Give the position of every Plasmodium parasite visible.
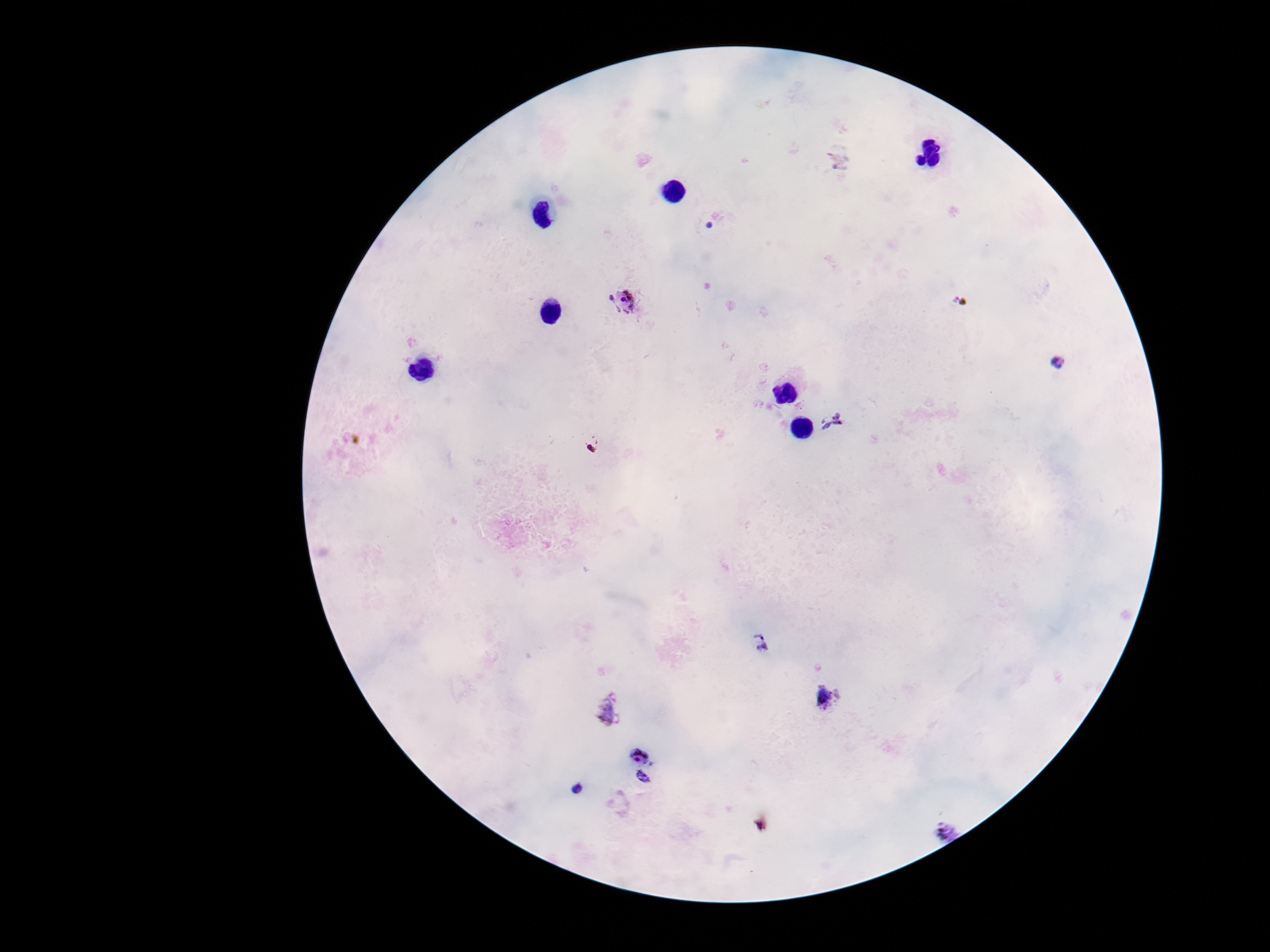
Approximate centers as {x, y} in pixels.
Plasmodium parasites: {840, 159}, {624, 302}, {1058, 363}, {829, 421}, {762, 645}, {828, 697}, {609, 712}, {641, 754}, {645, 780}, {578, 790}, {941, 828}.

Summary:
  - Field of view: single
  - Patient malaria status: infected
  - Capture: smartphone camera through the microscope eyepiece
  - Magnification: 100x
  - Preparation: thick blood film
  - Image size: 1270×952 pixels
  - Stain: Giemsa